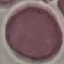

result = negative for malaria parasites
preparation = thin blood smear
capture = smartphone through the microscope eyepiece
image type = automatically extracted cell patch, resized to 64 × 64 pixels
stain = Giemsa